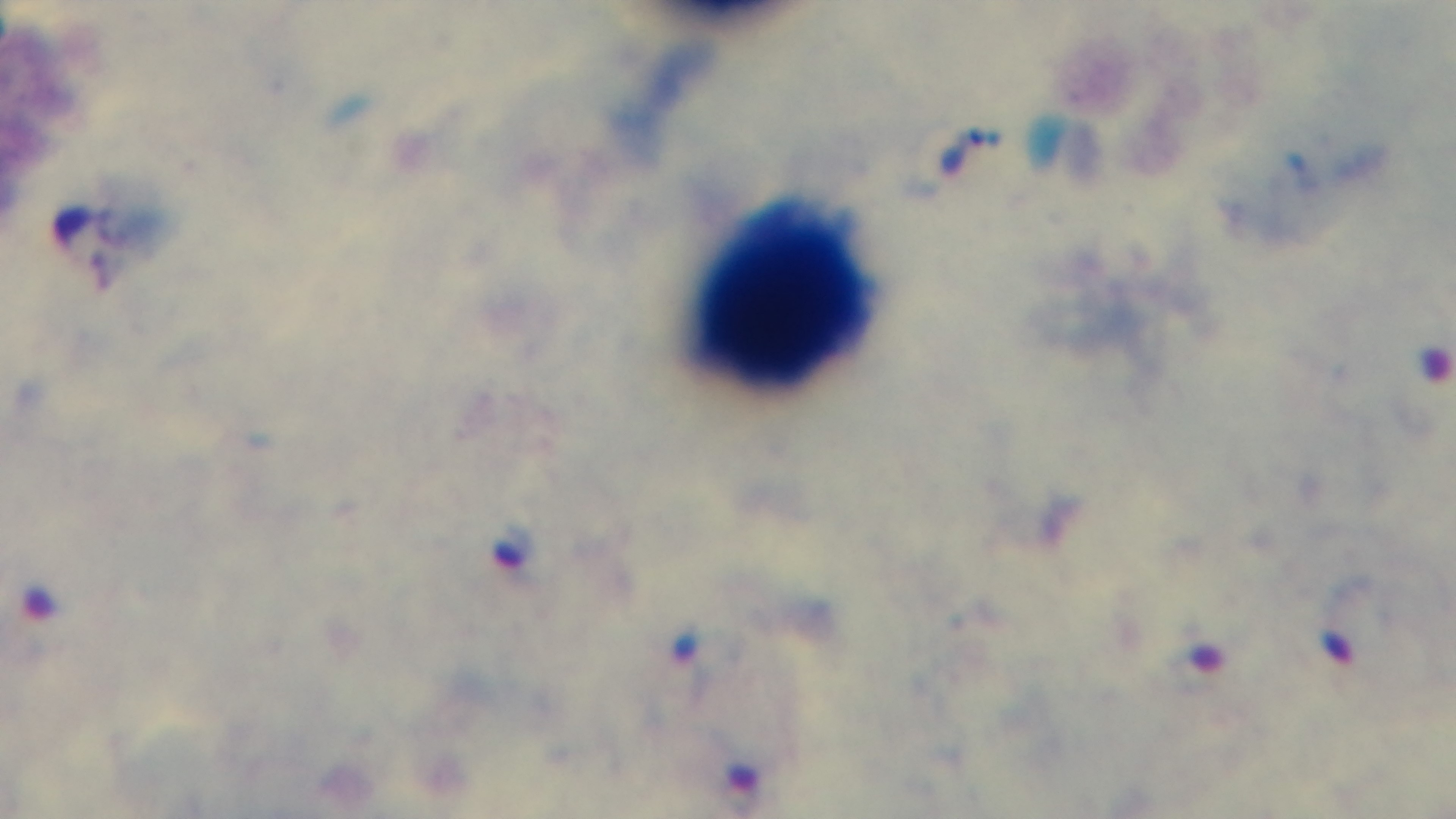

capture = mounted 4K digital camera
stain = Giemsa
malaria status = positive
preparation = thick smear
objective = 100x oil immersion
field of view = single
modality = light microscopy